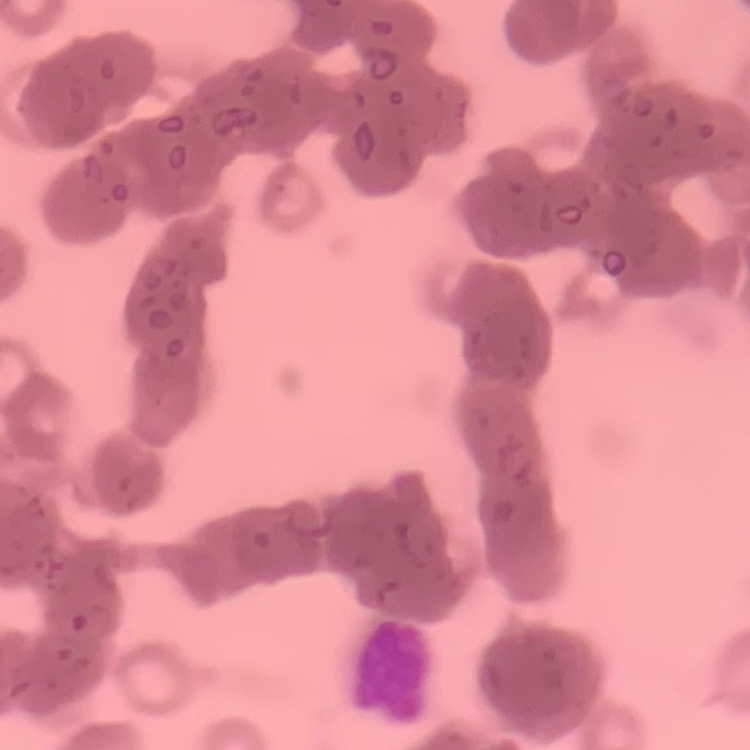
red blood cell morphology = rouleaux formation
stain = Field's or Giemsa
image type = square crop of a larger photomicrograph
preparation = thin blood smear